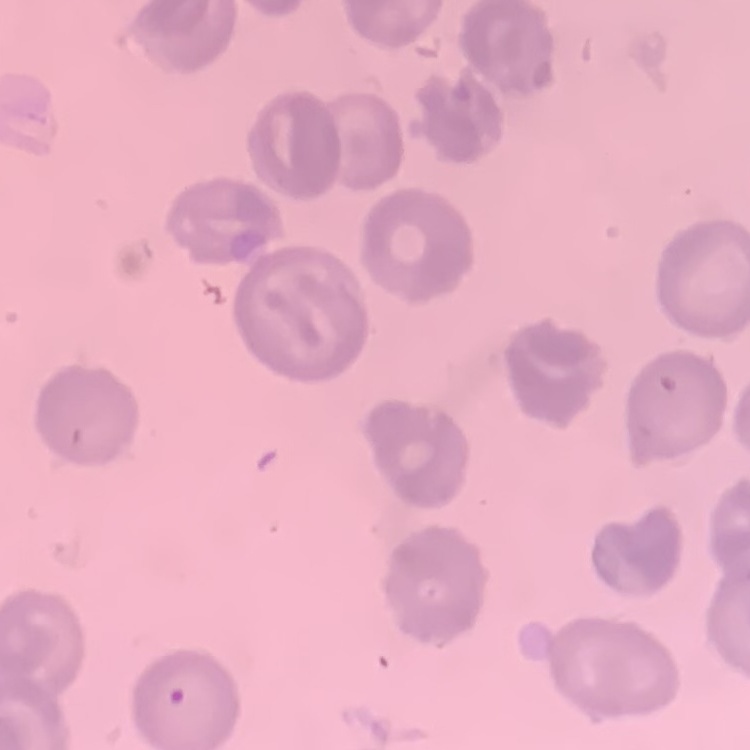
The red blood cells show no rouleaux formation. One tile cut from a larger photomicrograph. Field's or Giemsa stain. Thin blood smear.